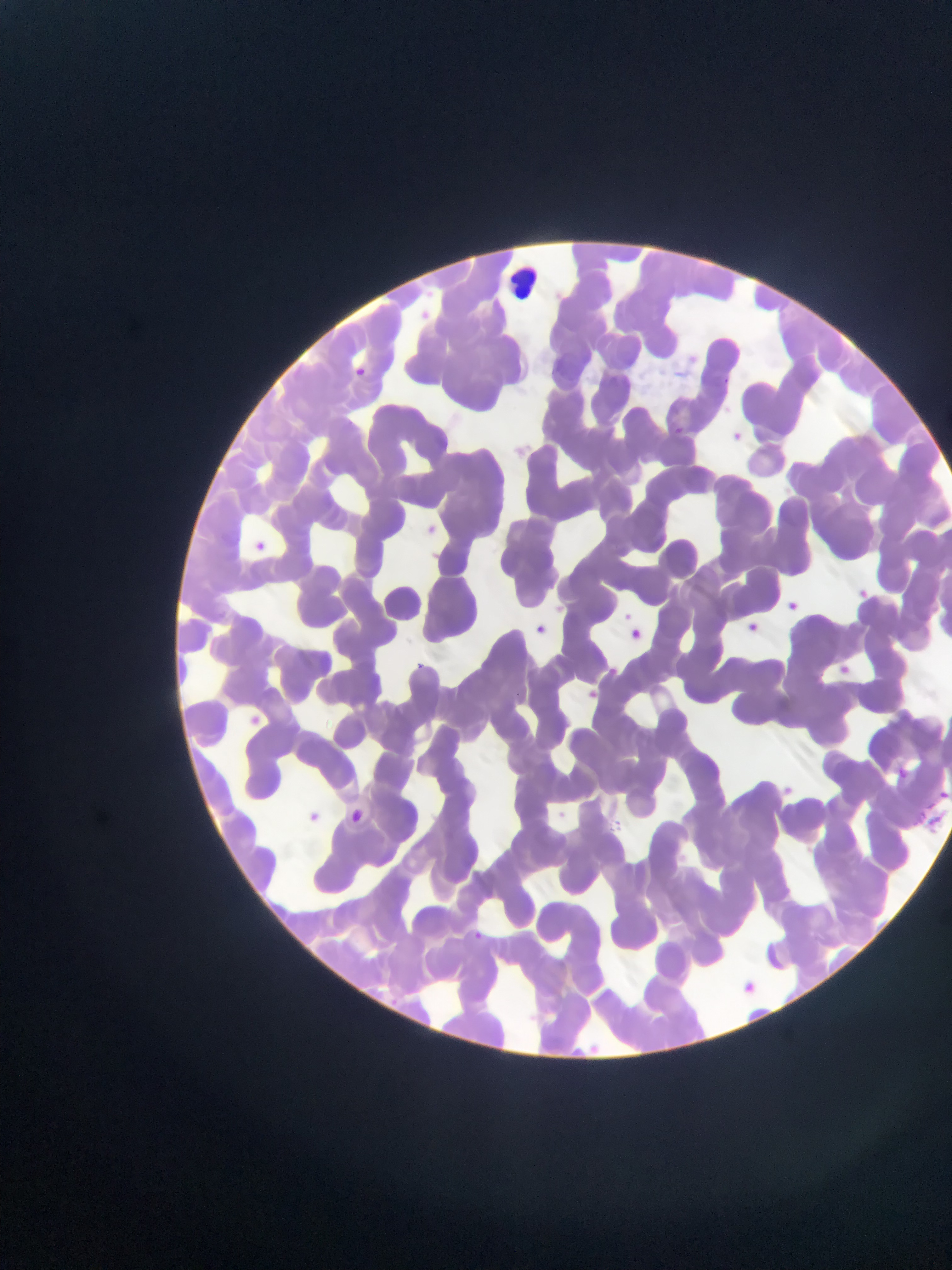 Approximate bounding boxes as left top right bottom in pixels. Plasmodium parasite locations: 412 297 440 326; 353 360 368 380; 671 414 690 439; 729 420 757 452; 517 434 539 462; 414 517 457 545; 253 534 275 555; 849 579 865 597; 784 596 799 611; 610 609 658 657; 533 610 553 641; 745 612 760 635; 837 660 859 680; 602 665 629 678; 579 678 601 706; 250 710 290 748; 887 763 908 783; 777 774 825 812; 940 786 952 803; 294 798 329 823; 349 804 394 831; 468 924 495 943; 743 976 773 996. Leukocyte locations: 484 255 552 298. Image is 952×1270 pixels. Thin blood smear. Sample from Ghana. Single field of view. Photographed through a microscope with a mobile-phone camera.